Comment on the morphology of the erythrocytes.
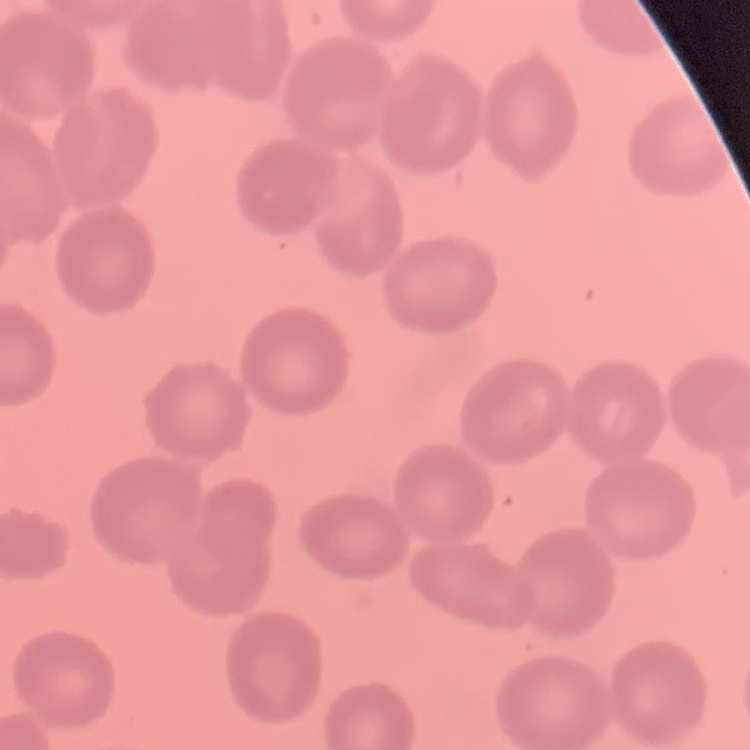
They show no rouleaux formation.

Stained with either Field's or Giemsa. Square crop of a larger photomicrograph. Thin blood smear.